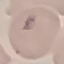

Summary:
  - Malaria status: uninfected
  - Stain: Giemsa
  - Image type: automatically extracted cell patch, resized to 64 × 64 pixels
  - Capture: smartphone camera at the microscope eyepiece
  - Preparation: thin smear